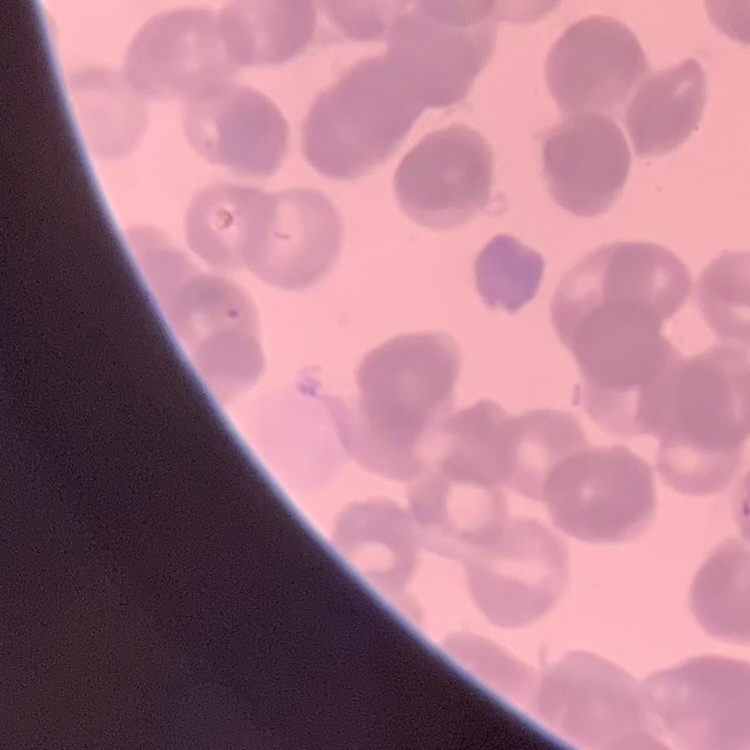

The red blood cells show rouleaux formation. Stained with either Field's or Giemsa. Square crop of a larger photomicrograph. Thin peripheral smear.